Report the malaria status of this cell.
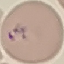
Parasitized.

Giemsa stain. Cell patch, automatically extracted from a larger field of view and resized to 64 × 64 pixels. Photographed with a smartphone camera at the microscope eyepiece. Thin smear of blood.